Name the parasite shown.
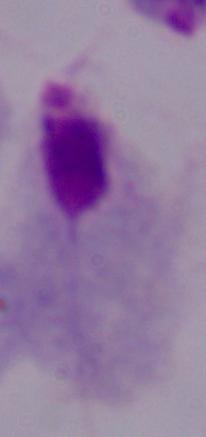
A trichomonad.

modality: micrograph
magnification: 1000x